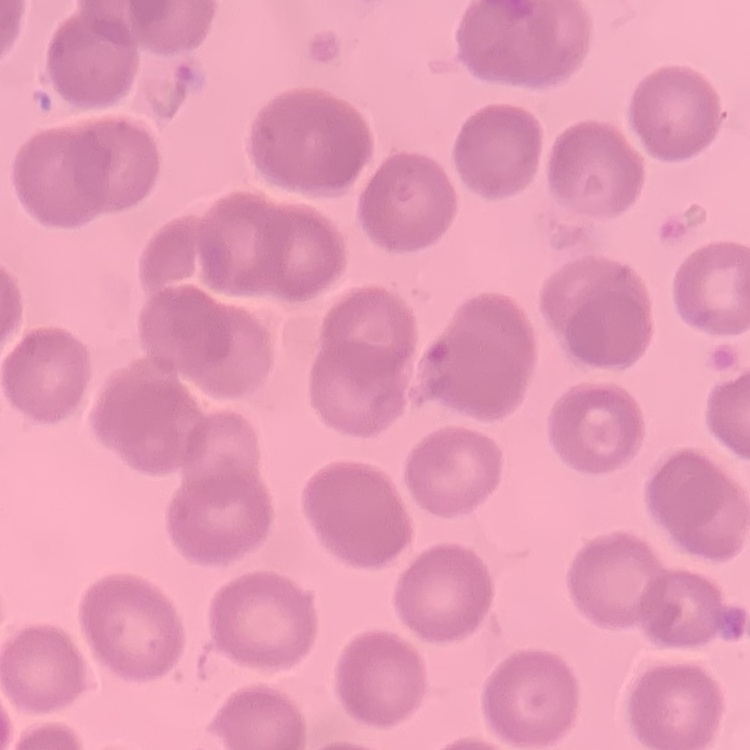
Summary:
  - Red blood cell morphology: no rouleaux formation
  - Stain: Field's or Giemsa
  - Preparation: thin blood film
  - Image type: square crop of a larger photomicrograph